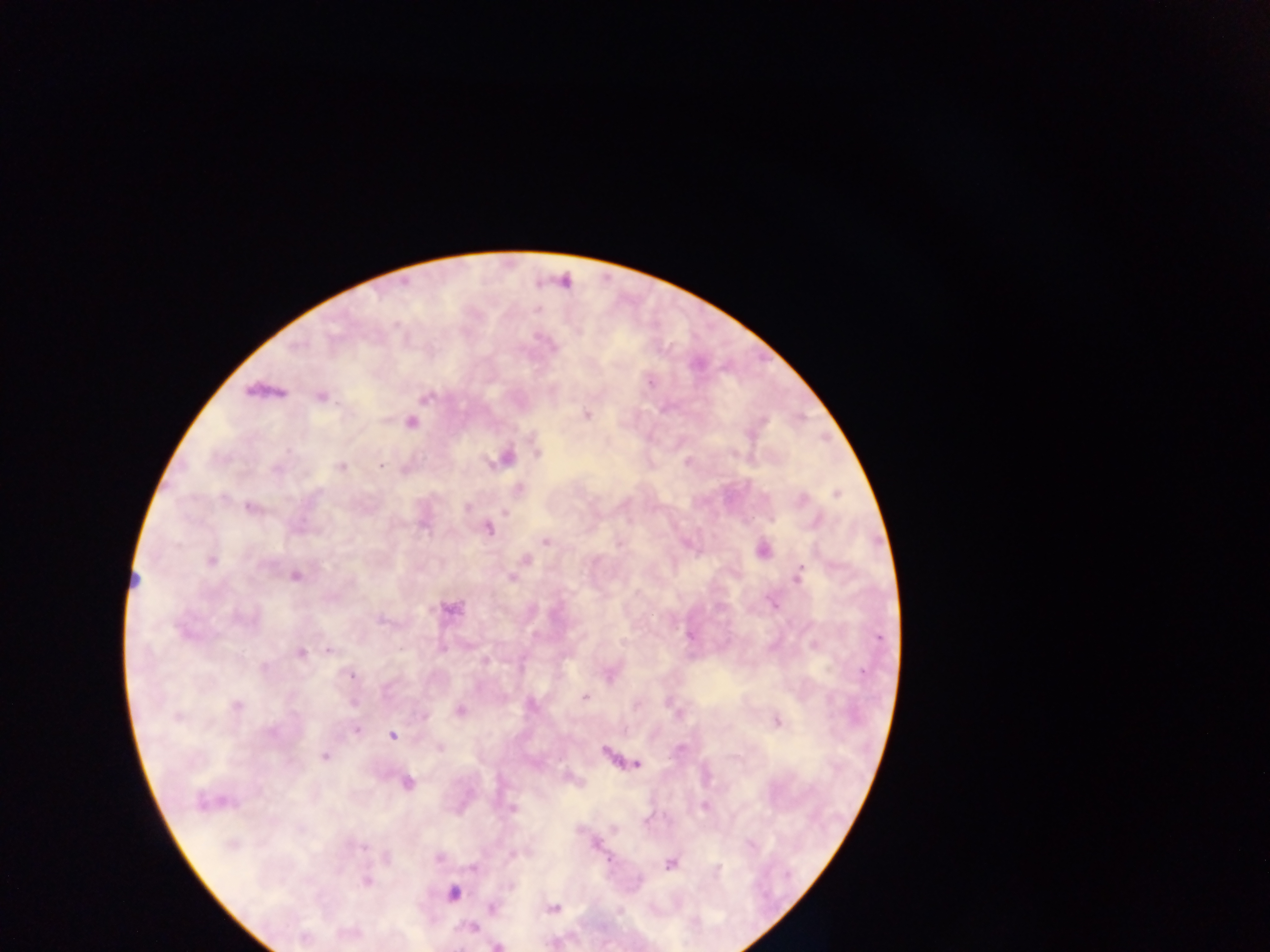

Approximate centers as [x, y] in pixels.
Summary:
  - Plasmodium parasite locations: [534, 310], [648, 381], [322, 396], [424, 397], [587, 416], [411, 423], [537, 453], [507, 456], [490, 463], [686, 463], [381, 466], [340, 467], [406, 469], [519, 488], [837, 495], [248, 505], [466, 508], [504, 512], [772, 521], [487, 529], [546, 541], [525, 558], [801, 568], [511, 578], [452, 610], [381, 621], [690, 636], [878, 638], [328, 649], [301, 653], [351, 675], [583, 696], [636, 705], [425, 717], [775, 721], [356, 730], [392, 736], [605, 750], [323, 757], [638, 765], [406, 785], [512, 808], [646, 821], [438, 859], [670, 864], [472, 866], [555, 908], [494, 909], [472, 928], [496, 945]
  - Field of view: single
  - Country: Ghana
  - Image size: 1270×952 pixels
  - Capture: mobile-phone photograph through a microscope
  - Preparation: thick blood smear